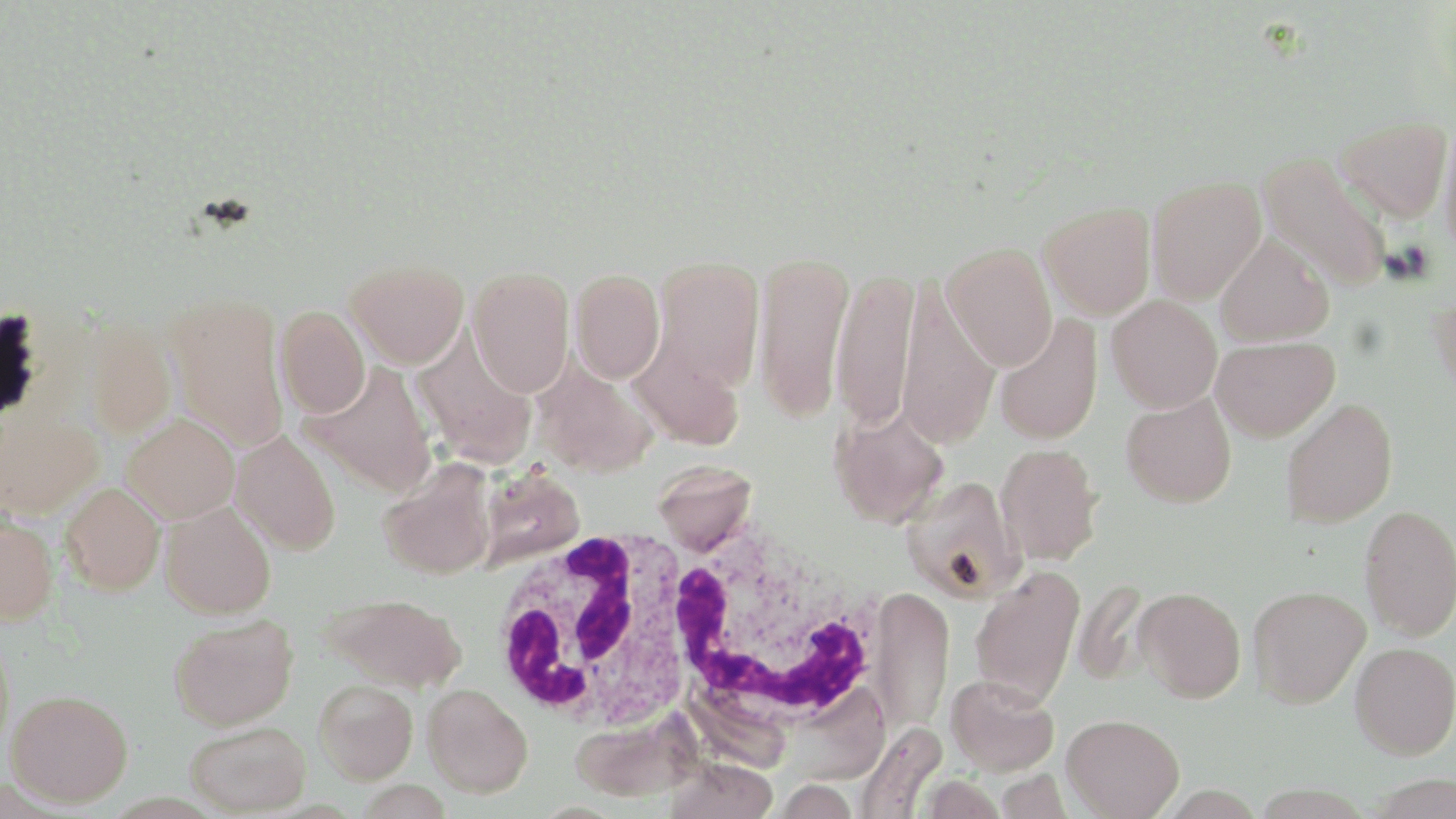
Approximate bounding boxes as (x1, y1, x2, y2) in pixels. White blood cell locations: (658, 516, 886, 734), (486, 529, 707, 732). Uninfected red blood cell locations: (1334, 117, 1452, 222), (1438, 117, 1456, 260), (1257, 152, 1391, 292), (1147, 175, 1266, 304), (1039, 202, 1155, 320), (1215, 235, 1334, 347), (941, 241, 1057, 370), (754, 250, 854, 422), (650, 256, 765, 390), (345, 259, 468, 368), (830, 266, 918, 431), (467, 267, 574, 397), (570, 269, 665, 383), (896, 277, 999, 448), (165, 292, 290, 452), (1429, 293, 1456, 401), (1106, 295, 1222, 412), (276, 307, 370, 418), (994, 314, 1103, 445), (79, 316, 177, 439), (411, 333, 537, 468), (1211, 337, 1339, 441), (628, 338, 746, 451), (532, 361, 659, 478), (302, 363, 438, 498), (1121, 392, 1237, 508), (1281, 398, 1398, 528), (830, 405, 950, 528), (0, 410, 104, 520), (121, 413, 240, 523), (231, 430, 342, 556), (995, 443, 1103, 565), (377, 459, 498, 580), (653, 460, 756, 554), (480, 475, 584, 569), (901, 475, 1023, 601), (60, 482, 165, 595), (159, 501, 276, 619), (1359, 504, 1456, 641), (0, 514, 60, 625), (969, 565, 1085, 707), (1247, 585, 1370, 708), (868, 586, 954, 733), (1134, 586, 1246, 702), (321, 593, 467, 693), (168, 615, 298, 730), (0, 635, 15, 760), (1350, 642, 1456, 759), (946, 674, 1059, 776), (314, 679, 418, 784), (423, 684, 534, 797), (6, 689, 133, 807), (568, 711, 700, 803), (1062, 713, 1184, 818), (185, 721, 310, 815), (854, 723, 946, 819), (664, 756, 779, 819), (993, 768, 1073, 819). Slide-level diagnosis: Plasmodium falciparum. Thin blood smear. Light microscopy. May-Grünwald-Giemsa-stained preparation. Image is 1456×819 pixels. One field of a larger specimen. 1000x magnification.